Assess for Plasmodium parasites.
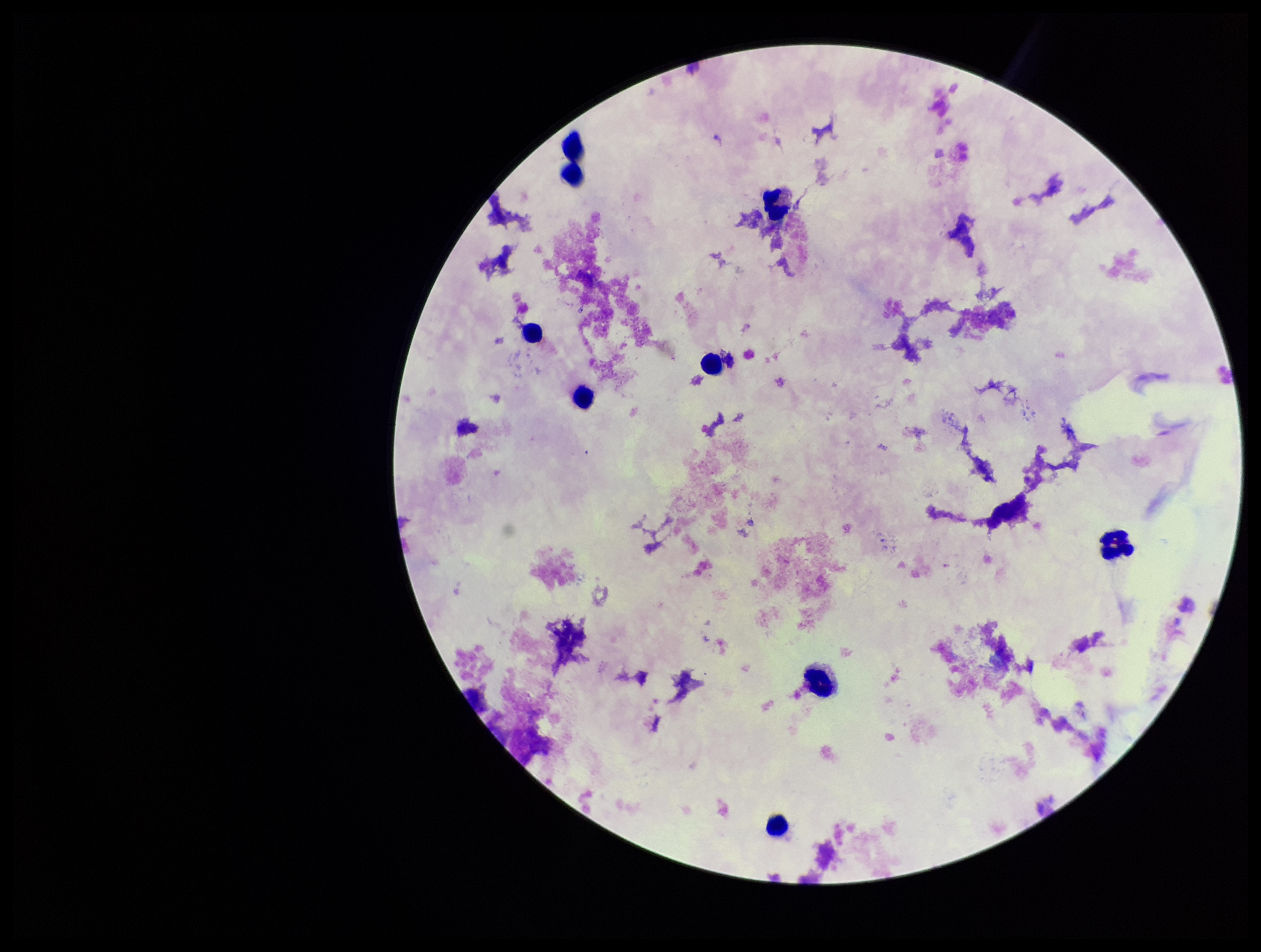

None detected.

capture = smartphone photograph through the microscope eyepiece
leukocyte count = 9
parasite count = 0
preparation = thick smear
stain = Giemsa
image size = 1261×952 pixels
patient malaria status = negative
field of view = single